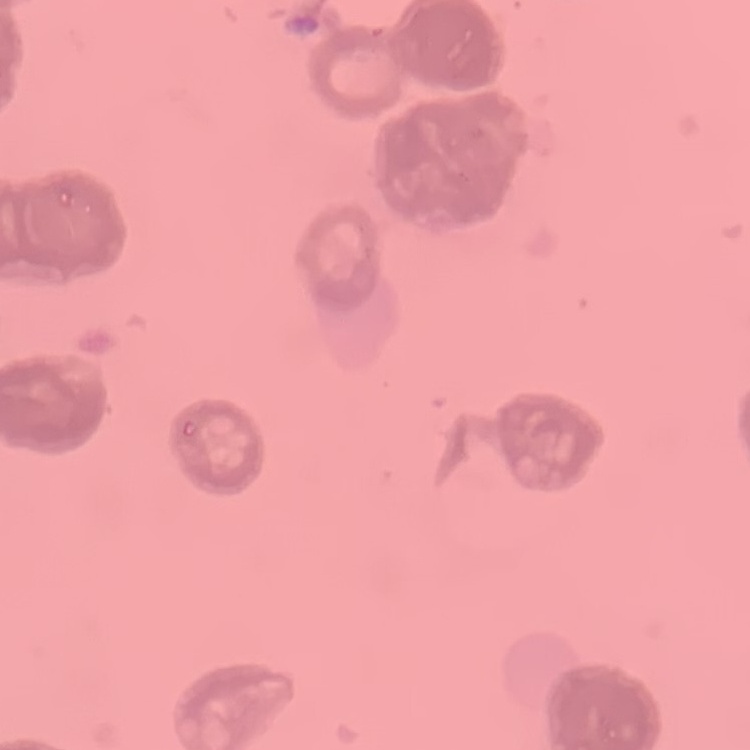

Summary:
  - Erythrocyte morphology: rouleaux formation
  - Preparation: thin blood film
  - Image type: one tile cut from a larger photomicrograph
  - Stain: Field's or Giemsa